Describe the morphology of the red blood cells.
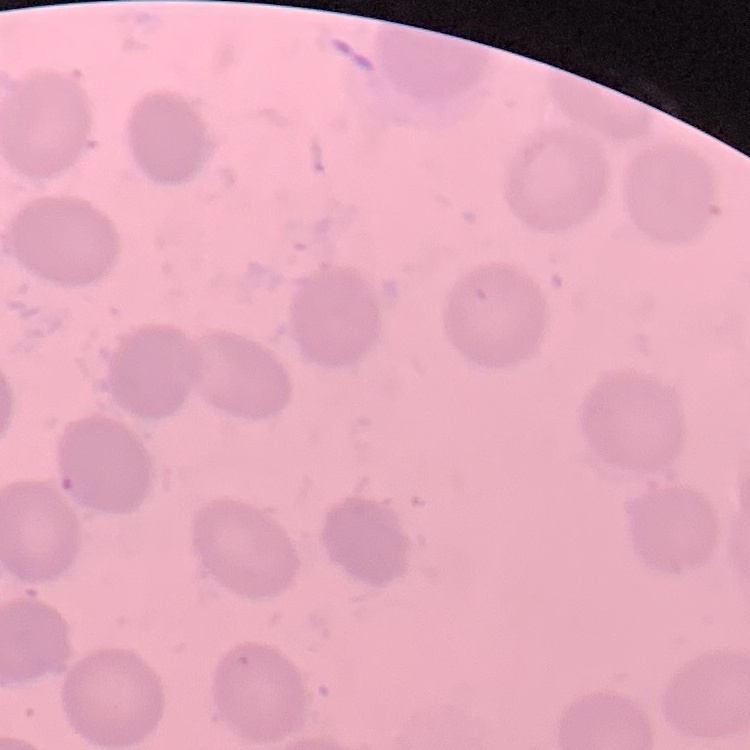

They show no rouleaux formation.

stain = Field's or Giemsa
image type = one tile cut from a larger photomicrograph
preparation = thin blood film